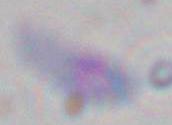

modality = micrograph
identification = Toxoplasma gondii
magnification = 1000x